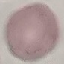
Result: no malaria parasites detected. Giemsa-stained preparation. Cell patch, automatically extracted from a larger field of view and resized to 64 × 64 pixels. Thin blood smear. Photographed with a smartphone camera at the microscope eyepiece.